Locate and identify every blood parasite.
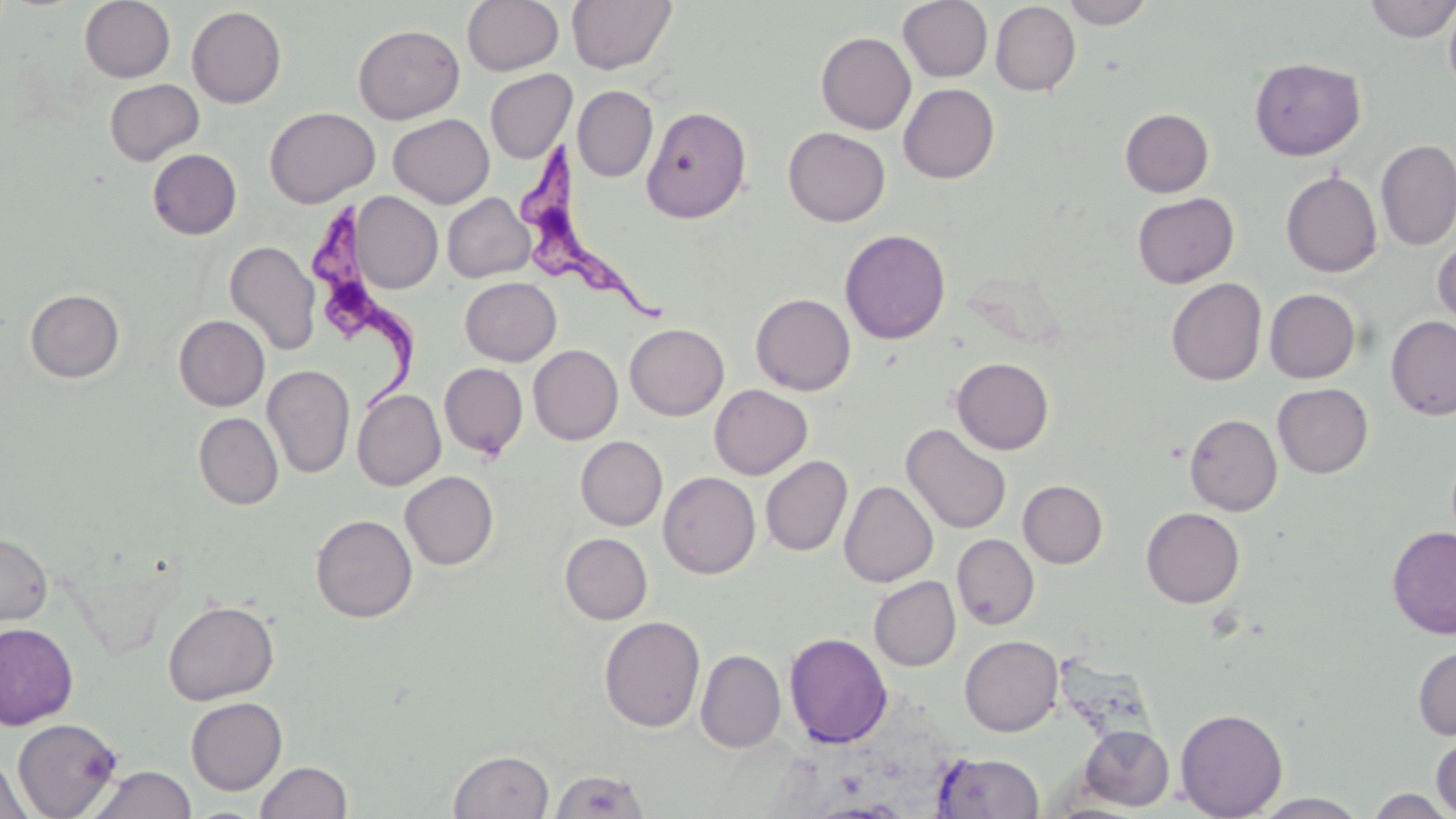

Approximate bounding boxes as (x1,y1)-(x2,y2) corner pairs in pixels.
Trypanosoma brucei: (523,145)-(677,328), (307,203)-(417,407).
No Plasmodium falciparum, Plasmodium ovale, Plasmodium malariae, Plasmodium vivax, or Babesia divergens observed.

Summary:
  - Uninfected red blood cell locations: (79,0)-(175,82), (462,0)-(564,75), (566,0)-(677,75), (897,0)-(993,82), (1061,0)-(1156,28), (1363,0)-(1456,42), (1443,0)-(1456,97), (990,2)-(1081,97), (187,6)-(286,108), (353,24)-(464,123), (816,31)-(916,134), (1249,57)-(1366,161), (485,69)-(577,163), (104,79)-(204,165), (898,83)-(1000,183), (572,85)-(657,182), (641,105)-(752,223), (265,106)-(380,208), (1119,108)-(1214,197), (388,113)-(494,208), (783,127)-(890,226), (1376,140)-(1456,250), (147,149)-(242,239), (1281,171)-(1382,277), (349,192)-(442,293), (442,192)-(535,282), (1133,192)-(1239,288), (840,228)-(951,345), (1432,236)-(1456,335), (225,240)-(321,356), (460,277)-(561,365), (1166,278)-(1267,385), (25,288)-(125,382), (1264,288)-(1360,383), (751,293)-(855,395), (174,315)-(269,411), (1386,316)-(1456,420), (624,323)-(729,421), (529,344)-(623,445), (952,357)-(1054,455), (439,363)-(528,460), (262,364)-(355,479), (1272,383)-(1373,478), (709,384)-(812,479), (352,389)-(446,491), (193,412)-(283,509), (1184,414)-(1282,515), (900,424)-(1012,535), (575,436)-(667,530), (761,455)-(853,556), (400,471)-(498,570), (658,471)-(761,579), (1018,479)-(1108,568), (839,481)-(938,587), (1141,507)-(1244,607), (310,514)-(417,623), (1387,526)-(1456,638), (0,532)-(53,626), (560,532)-(652,624), (952,534)-(1039,629), (869,576)-(961,671), (163,599)-(279,705), (599,615)-(705,732), (0,622)-(78,730), (6,624)-(94,817), (784,632)-(893,748), (960,635)-(1063,736), (1413,644)-(1456,741), (695,650)-(786,752), (186,697)-(287,794), (1175,708)-(1288,818), (13,718)-(123,818), (1078,724)-(1174,811), (1431,732)-(1456,818), (448,749)-(554,819), (932,752)-(1045,818), (1,755)-(31,819), (255,760)-(352,819), (88,765)-(197,819), (549,769)-(651,818), (1364,789)-(1455,818), (1252,793)-(1371,818)
  - Slide-level diagnosis: Trypanosoma brucei
  - Stain: May-Grünwald-Giemsa
  - Magnification: 1000x
  - Field of view: one of a larger specimen
  - Modality: light microscopy
  - Preparation: thin blood film
  - Image size: 1456×819 pixels